Describe the morphology of the erythrocytes.
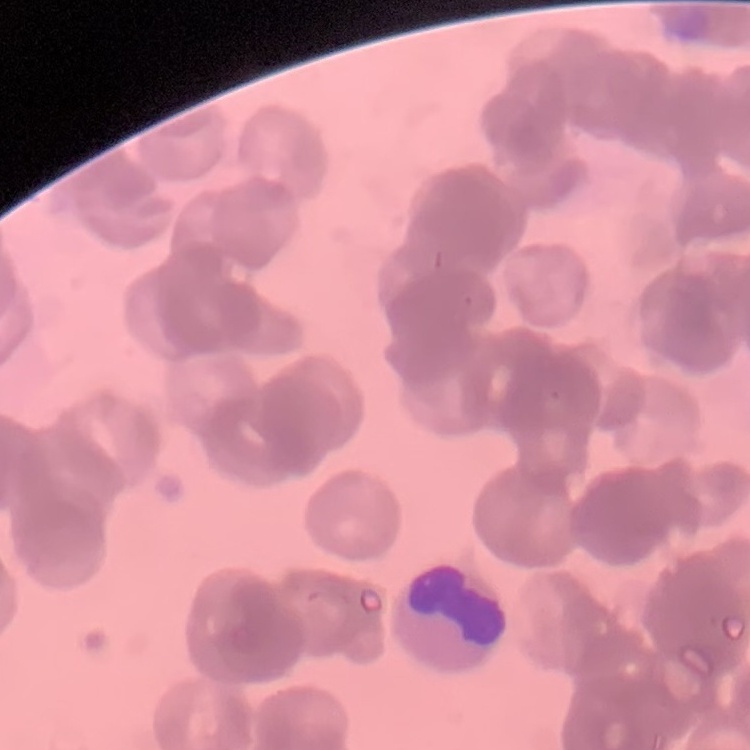
They show rouleaux formation.

image_type: one tile cut from a larger photomicrograph
preparation: thin blood smear
stain: Field's or Giemsa